State which parasite is depicted.
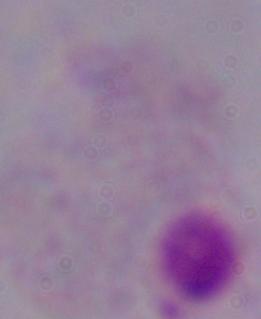

This is a trichomonad.

Micrograph. 1000x magnification.